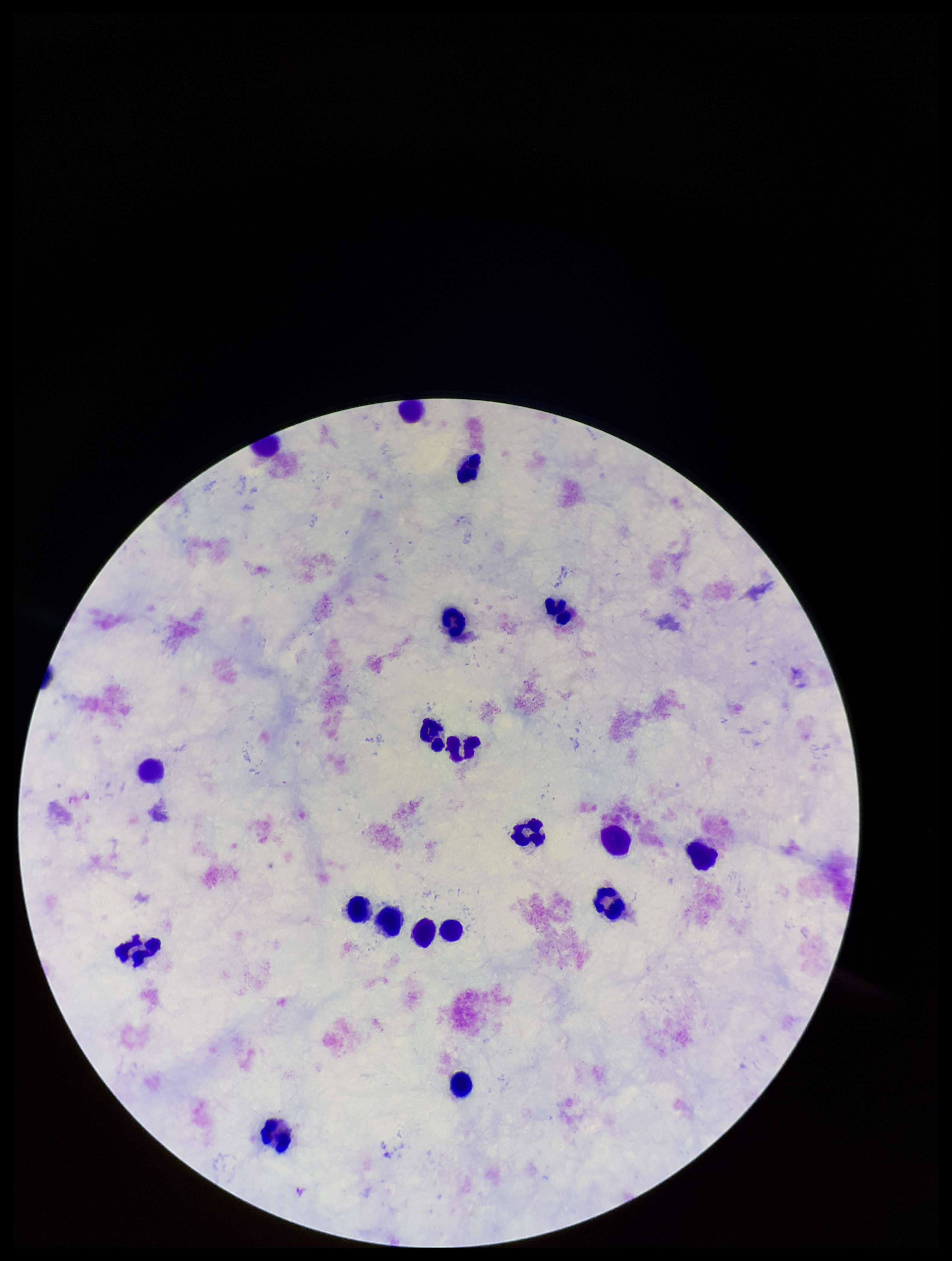

Summary:
  - Patient malaria status: negative
  - Leukocyte count: 19
  - Parasite count: 0
  - Capture: smartphone photograph through the microscope eyepiece
  - Field of view: one from this slide
  - Plasmodium parasites: none identified
  - Image size: 952×1261 pixels
  - Preparation: thick
  - Stain: Giemsa